Assess this cell for malaria.
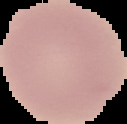
It is uninfected.

Image is 127×124 pixels. Cell region segmented out of the field of view; the surrounding area is masked to black. From a thin blood smear.